Report the malaria status.
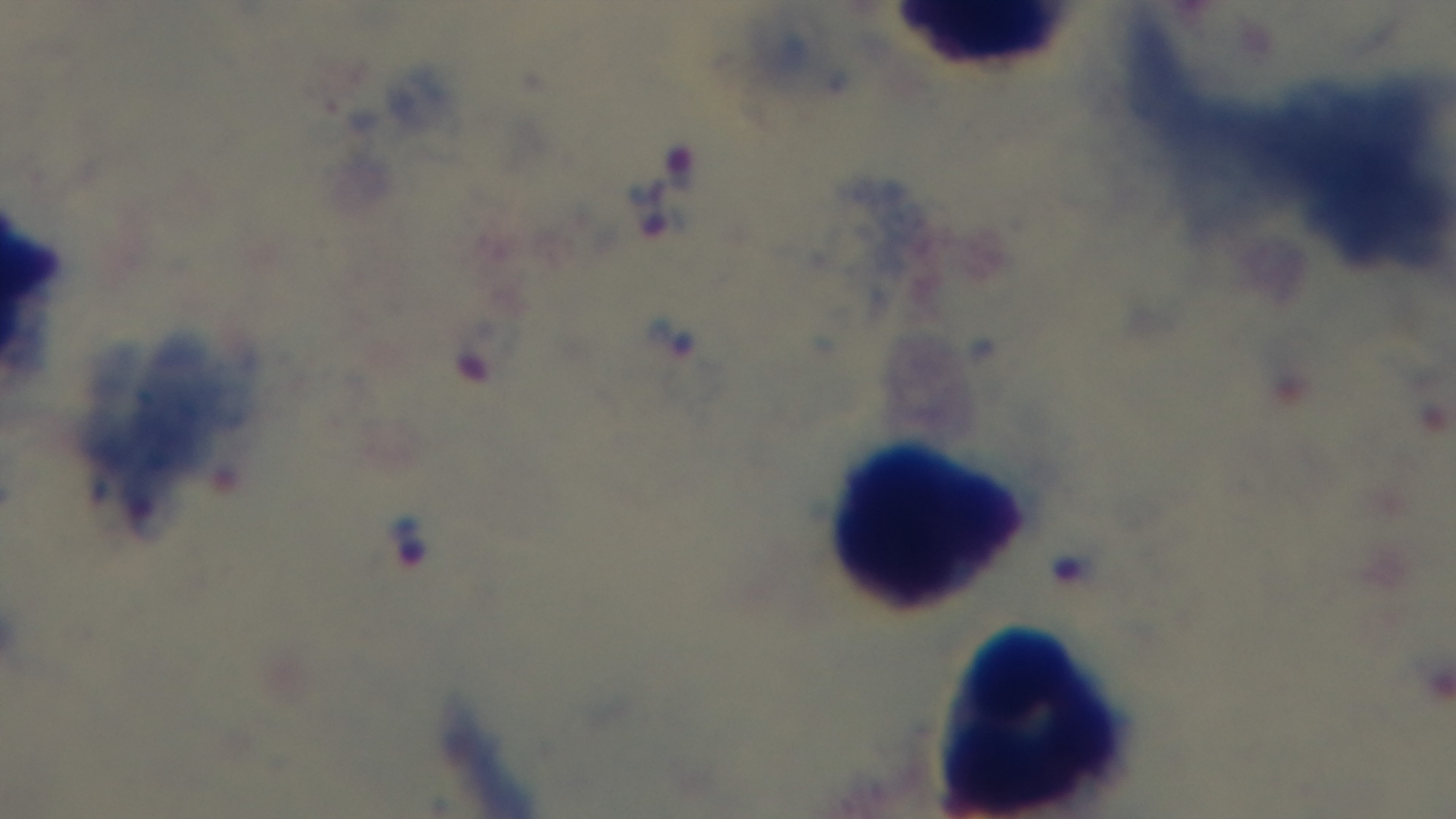
It is infected.

objective = 100x oil immersion
capture = mounted 4K digital camera
preparation = thick
stain = Giemsa
modality = light microscopy
field of view = single